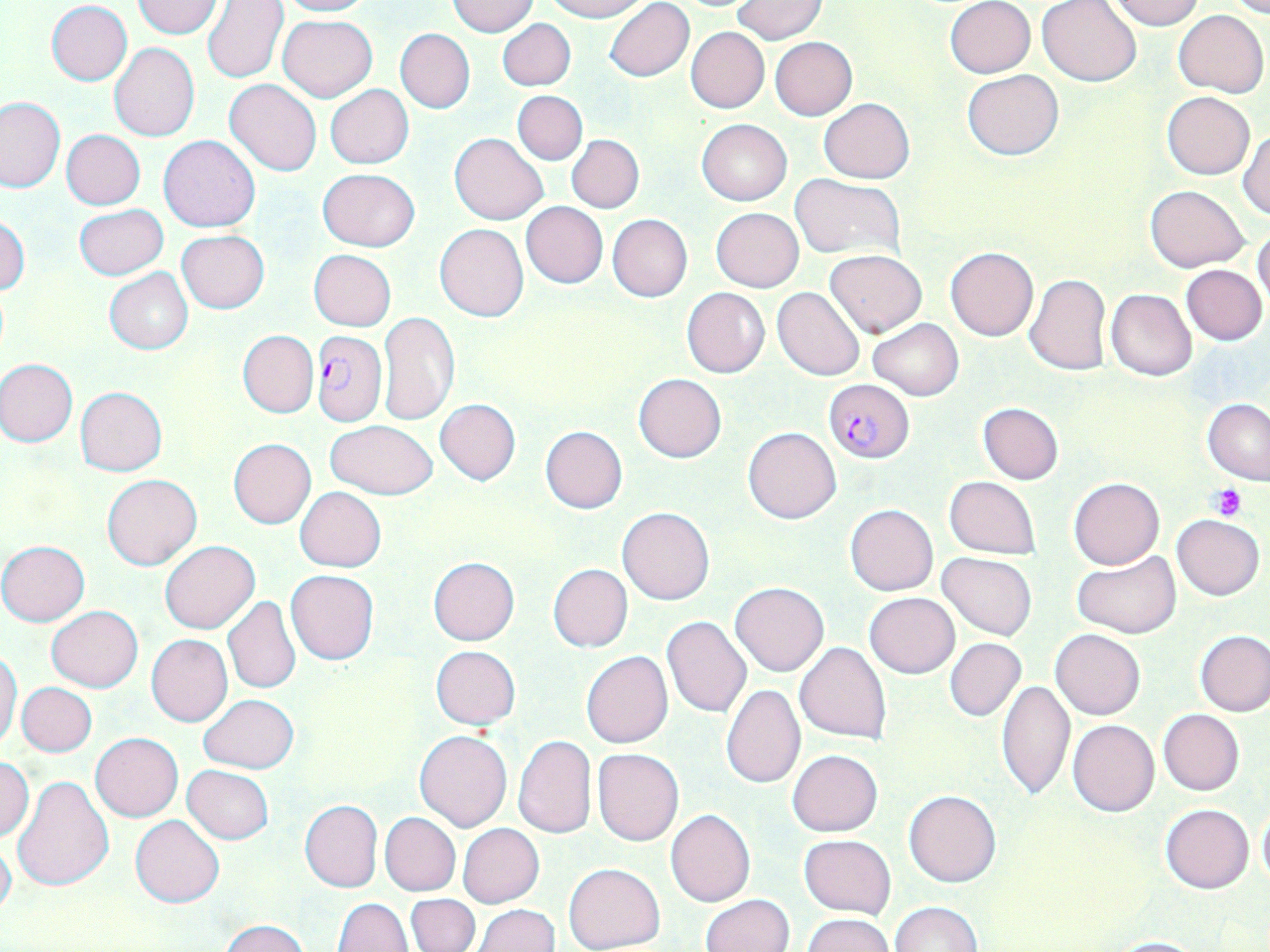
Summary:
  - Coordinate format: approximate bounding boxes as [x1, y1, x2, y2] in pixels
  - Plasmodium falciparum-infected red blood cell locations: [310, 331, 385, 427], [823, 379, 913, 463]
  - Platelet locations: [1211, 485, 1247, 519]
  - Uninfected red blood cell locations: [132, 0, 223, 39], [275, 0, 373, 17], [544, 0, 649, 21], [951, 0, 1044, 158], [1108, 0, 1203, 30], [1217, 0, 1270, 16], [203, 1, 288, 84], [448, 1, 538, 37], [603, 1, 694, 81], [733, 1, 826, 43], [944, 1, 1035, 78], [1037, 1, 1142, 85], [47, 2, 132, 85], [60, 8, 169, 111], [1172, 9, 1268, 97], [278, 15, 376, 102], [498, 19, 575, 91], [686, 27, 769, 113], [395, 28, 474, 113], [770, 37, 857, 120], [109, 43, 199, 142], [961, 70, 1064, 160], [225, 79, 321, 176], [325, 85, 414, 168], [513, 90, 587, 165], [1162, 91, 1255, 180], [0, 97, 64, 193], [818, 98, 914, 182], [697, 118, 791, 206], [1237, 128, 1269, 219], [61, 129, 145, 210], [450, 133, 549, 225], [567, 134, 644, 214], [159, 136, 261, 232], [317, 168, 421, 251], [790, 175, 905, 261], [1145, 185, 1249, 272], [521, 202, 608, 288], [75, 203, 168, 280], [710, 207, 805, 292], [607, 213, 692, 301], [0, 217, 29, 295], [435, 224, 527, 321], [1252, 226, 1270, 307], [177, 230, 269, 313], [945, 246, 1038, 341], [309, 249, 395, 331], [824, 249, 927, 337], [1182, 265, 1267, 344], [104, 267, 193, 354], [1024, 273, 1112, 375], [682, 287, 771, 379], [773, 287, 866, 382], [1106, 289, 1195, 380], [378, 311, 461, 427], [869, 318, 964, 401], [237, 330, 318, 418], [1, 359, 78, 446], [634, 373, 726, 463], [75, 387, 168, 475], [1203, 399, 1270, 484], [435, 400, 521, 486], [979, 402, 1063, 484], [325, 420, 437, 499], [539, 426, 627, 514], [741, 426, 841, 523], [227, 438, 317, 528], [102, 473, 202, 570], [944, 475, 1040, 558], [1069, 476, 1163, 568], [295, 487, 386, 571], [845, 505, 938, 596], [617, 506, 715, 605], [1172, 514, 1265, 601], [0, 541, 90, 626], [160, 541, 259, 634], [1071, 551, 1179, 639], [937, 552, 1037, 640], [428, 556, 520, 645], [559, 558, 645, 726], [548, 564, 633, 652], [286, 569, 379, 665], [730, 582, 829, 676], [864, 592, 959, 678], [222, 596, 302, 695], [47, 606, 143, 692], [661, 617, 752, 720], [1050, 628, 1145, 719], [1195, 629, 1270, 717], [146, 634, 233, 726], [945, 638, 1025, 721], [795, 641, 892, 743], [431, 646, 521, 729], [581, 651, 673, 750], [0, 652, 22, 749], [997, 679, 1075, 801], [17, 682, 97, 757], [720, 684, 805, 788], [198, 694, 299, 773], [1158, 708, 1244, 795], [1078, 714, 1245, 804], [1069, 719, 1160, 816], [415, 729, 512, 832], [90, 732, 183, 821], [513, 734, 596, 838], [593, 747, 683, 846], [786, 749, 883, 836], [1, 756, 34, 842], [182, 765, 273, 844], [11, 773, 113, 890], [904, 789, 1002, 887], [299, 800, 383, 892], [1160, 804, 1254, 893], [1257, 808, 1270, 887], [664, 809, 756, 907], [380, 812, 461, 895], [130, 815, 224, 907], [458, 823, 543, 908], [799, 835, 896, 918], [0, 836, 17, 920], [564, 863, 666, 952], [405, 894, 479, 952], [702, 894, 794, 952], [334, 899, 413, 952], [888, 901, 982, 952], [473, 904, 559, 951], [802, 913, 894, 952], [219, 919, 311, 952], [1103, 936, 1209, 951]
  - Slide-level diagnosis: Plasmodium falciparum
  - Stain: May-Grünwald-Giemsa
  - Image size: 1270×952 pixels
  - Preparation: thin blood smear
  - Magnification: 1000x
  - Field of view: one of a larger specimen
  - Modality: light microscopy